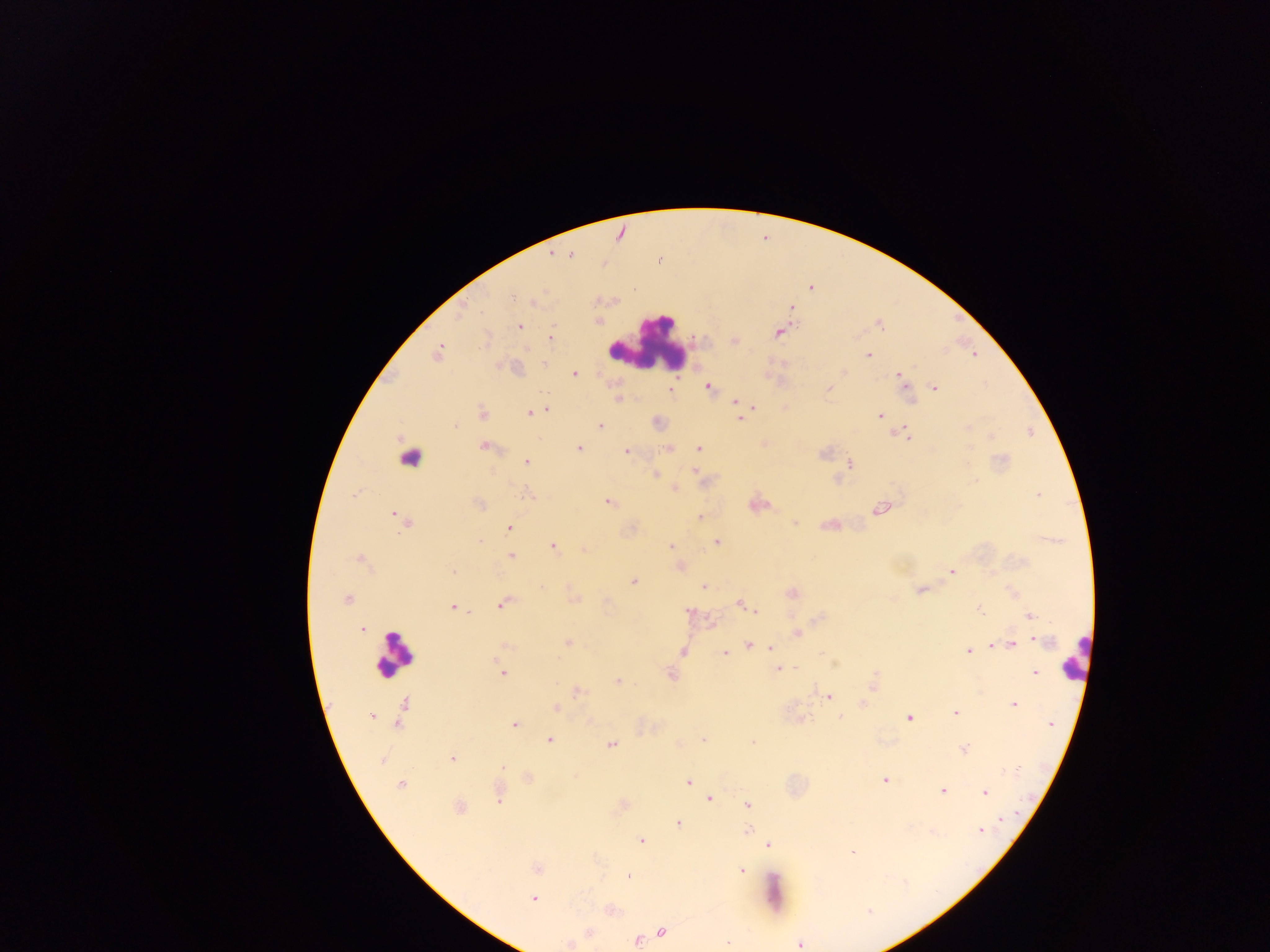 Approximate centers as {x, y} in pixels. Leukocyte locations: {647, 346}, {410, 457}, {393, 653}, {1075, 657}, {773, 889}. Plasmodium parasite locations: {571, 256}, {660, 261}, {811, 288}, {512, 297}, {791, 308}, {878, 325}, {519, 326}, {779, 332}, {550, 338}, {734, 341}, {437, 353}, {973, 354}, {868, 355}, {545, 364}, {844, 372}, {574, 373}, {899, 375}, {708, 387}, {935, 388}, {827, 389}, {669, 390}, {735, 402}, {752, 406}, {546, 410}, {482, 413}, {529, 413}, {879, 415}, {739, 418}, {455, 426}, {600, 426}, {904, 434}, {991, 436}, {485, 447}, {579, 448}, {669, 448}, {698, 449}, {626, 451}, {823, 454}, {526, 461}, {849, 464}, {694, 471}, {655, 475}, {675, 489}, {1038, 494}, {527, 495}, {608, 502}, {476, 504}, {881, 508}, {396, 515}, {700, 517}, {405, 522}, {794, 523}, {509, 528}, {479, 540}, {716, 542}, {670, 546}, {554, 547}, {583, 550}, {511, 556}, {360, 559}, {453, 571}, {951, 572}, {633, 581}, {703, 587}, {920, 590}, {347, 600}, {740, 603}, {503, 604}, {453, 607}, {980, 610}, {689, 611}, {756, 612}, {1029, 616}, {362, 629}, {798, 633}, {1040, 641}, {567, 643}, {993, 644}, {1013, 644}, {748, 645}, {770, 648}, {683, 652}, {968, 652}, {724, 653}, {796, 667}, {779, 668}, {503, 673}, {670, 673}, {1035, 674}, {617, 682}, {579, 691}, {828, 696}, {403, 704}, {1014, 705}, {557, 708}, {955, 713}, {371, 715}, {840, 717}, {908, 717}, {398, 723}, {515, 724}, {1050, 724}, {702, 739}, {549, 740}, {753, 743}, {610, 745}, {964, 749}, {382, 760}, {452, 760}, {504, 767}, {884, 780}, {688, 782}, {400, 785}, {942, 791}, {985, 793}, {499, 797}, {709, 799}, {747, 805}, {459, 808}, {1000, 820}, {678, 823}, {747, 830}, {980, 831}, {641, 841}, {768, 845}, {852, 851}, {536, 869}, {741, 870}, {629, 875}, {534, 898}, {869, 911}, {662, 932}, {637, 940}, {727, 942}, {569, 944}, {800, 945}. Thick blood film. Image is 1270×952 pixels. Collected in Ghana. One field of view. Mobile-phone photograph taken through the microscope.